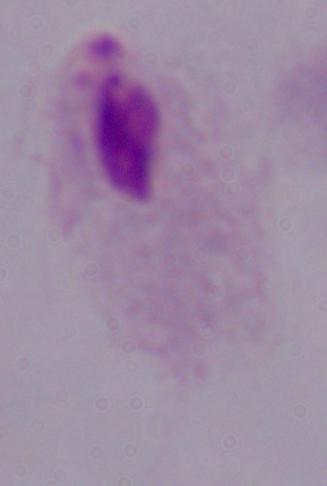
Summary:
  - Magnification: 1000x
  - Modality: photomicrograph
  - Identification: trichomonad